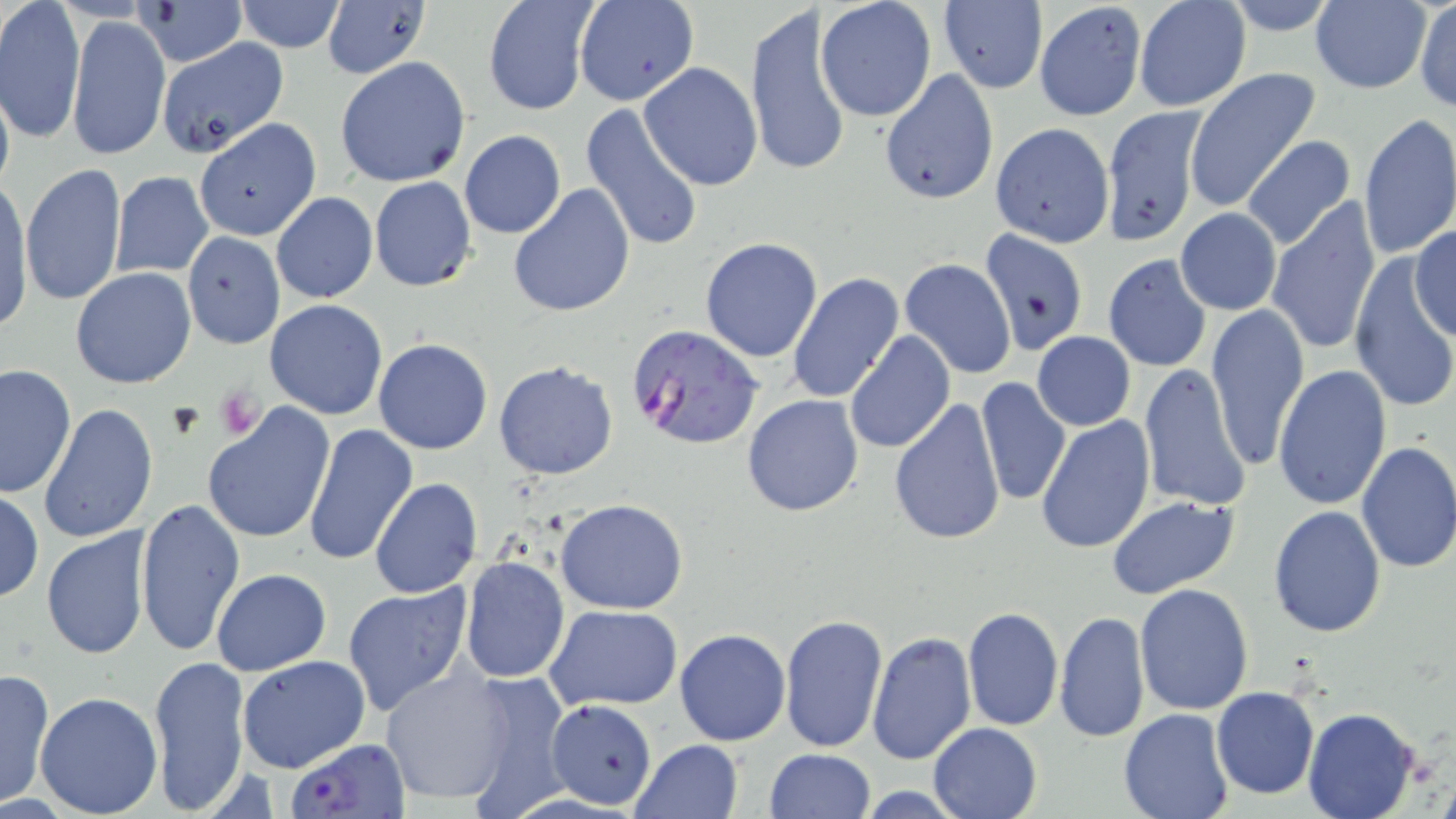

Summary:
  - Coordinate format: approximate bounding boxes as (x1, y1, x2, y2) in pixels
  - Plasmodium falciparum-infected red blood cell locations: (628, 322, 764, 452), (289, 736, 408, 819)
  - Platelet locations: (216, 387, 265, 439), (166, 403, 206, 440)
  - Uninfected red blood cell locations: (1, 0, 85, 142), (139, 0, 247, 69), (324, 0, 430, 81), (575, 0, 699, 106), (814, 0, 937, 122), (1034, 0, 1146, 122), (1134, 0, 1250, 112), (235, 1, 346, 52), (937, 1, 1049, 93), (1414, 1, 1456, 113), (482, 2, 597, 116), (1308, 2, 1433, 93), (744, 5, 852, 180), (68, 13, 169, 161), (156, 38, 289, 157), (335, 56, 471, 189), (638, 62, 762, 191), (1184, 67, 1319, 213), (878, 71, 999, 206), (0, 73, 16, 199), (579, 102, 705, 254), (1101, 105, 1205, 248), (1358, 113, 1456, 261), (195, 118, 321, 241), (989, 123, 1114, 247), (459, 131, 566, 240), (1242, 136, 1357, 253), (20, 162, 126, 306), (110, 171, 214, 277), (1, 176, 33, 332), (369, 177, 476, 291), (509, 185, 635, 318), (271, 193, 377, 305), (1267, 196, 1381, 355), (1175, 209, 1282, 315), (1410, 226, 1456, 337), (182, 231, 284, 349), (978, 231, 1088, 357), (698, 237, 823, 362), (1104, 254, 1212, 373), (1349, 257, 1454, 414), (898, 259, 1017, 382), (70, 266, 196, 389), (786, 271, 905, 403), (264, 299, 389, 419), (1206, 304, 1308, 470), (844, 331, 955, 456), (1032, 332, 1136, 430), (373, 337, 493, 455), (494, 358, 618, 480), (1139, 363, 1251, 513), (1, 365, 76, 500), (1275, 365, 1392, 511), (977, 377, 1071, 507), (741, 393, 864, 517), (889, 399, 1006, 548), (40, 404, 159, 543), (202, 404, 334, 542), (1035, 415, 1156, 554), (302, 422, 416, 566), (1355, 440, 1456, 573), (370, 478, 483, 600), (0, 487, 43, 603), (1106, 494, 1240, 600), (134, 497, 246, 656), (555, 498, 689, 614), (1268, 506, 1387, 637), (41, 527, 154, 662), (460, 555, 570, 685), (211, 569, 331, 676), (342, 581, 473, 717), (1134, 585, 1254, 716), (544, 605, 681, 711), (961, 606, 1063, 731), (780, 612, 888, 754), (1055, 613, 1149, 742), (675, 628, 791, 746), (867, 631, 976, 765), (148, 652, 251, 813), (238, 656, 369, 773), (0, 666, 55, 808), (380, 668, 517, 807), (458, 672, 575, 815), (1211, 687, 1319, 799), (35, 690, 163, 816), (545, 699, 657, 810), (1119, 707, 1233, 819), (1302, 708, 1422, 819), (928, 722, 1042, 819), (631, 738, 745, 819), (763, 748, 875, 819)
  - Slide-level diagnosis: Plasmodium falciparum
  - Image size: 1456×819 pixels
  - Magnification: 1000x
  - Preparation: thin blood smear
  - Modality: optical microscopy
  - Field of view: one of a larger specimen
  - Stain: May-Grünwald-Giemsa